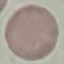

Summary:
  - Malaria status: uninfected
  - Capture: smartphone camera at the microscope eyepiece
  - Stain: Giemsa
  - Preparation: thin blood smear
  - Image type: automatically extracted cell patch, resized to 64 × 64 pixels